Assess the morphology of the red blood cells.
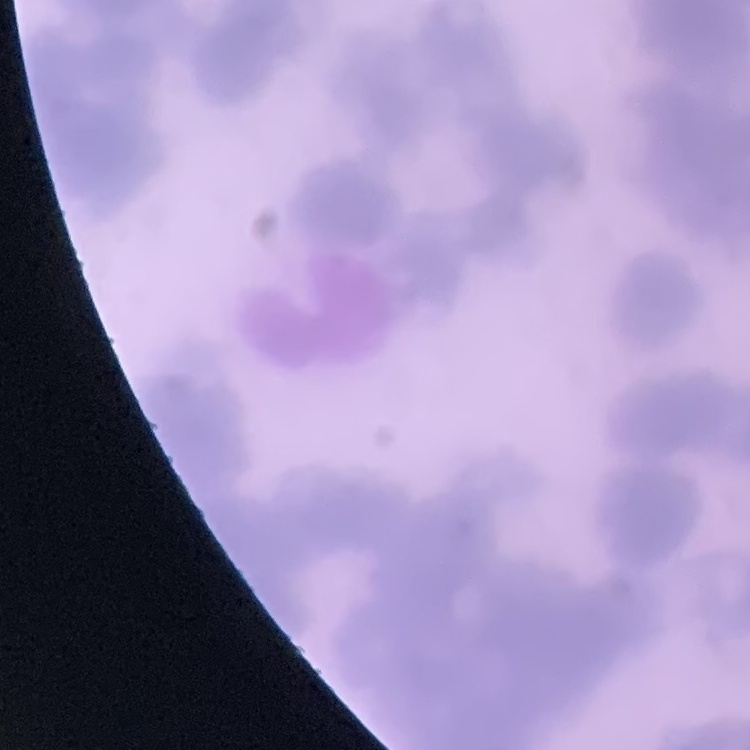

Rouleaux formation.

Summary:
  - Image type: square crop of a larger photomicrograph
  - Stain: Field's or Giemsa
  - Preparation: thin blood smear